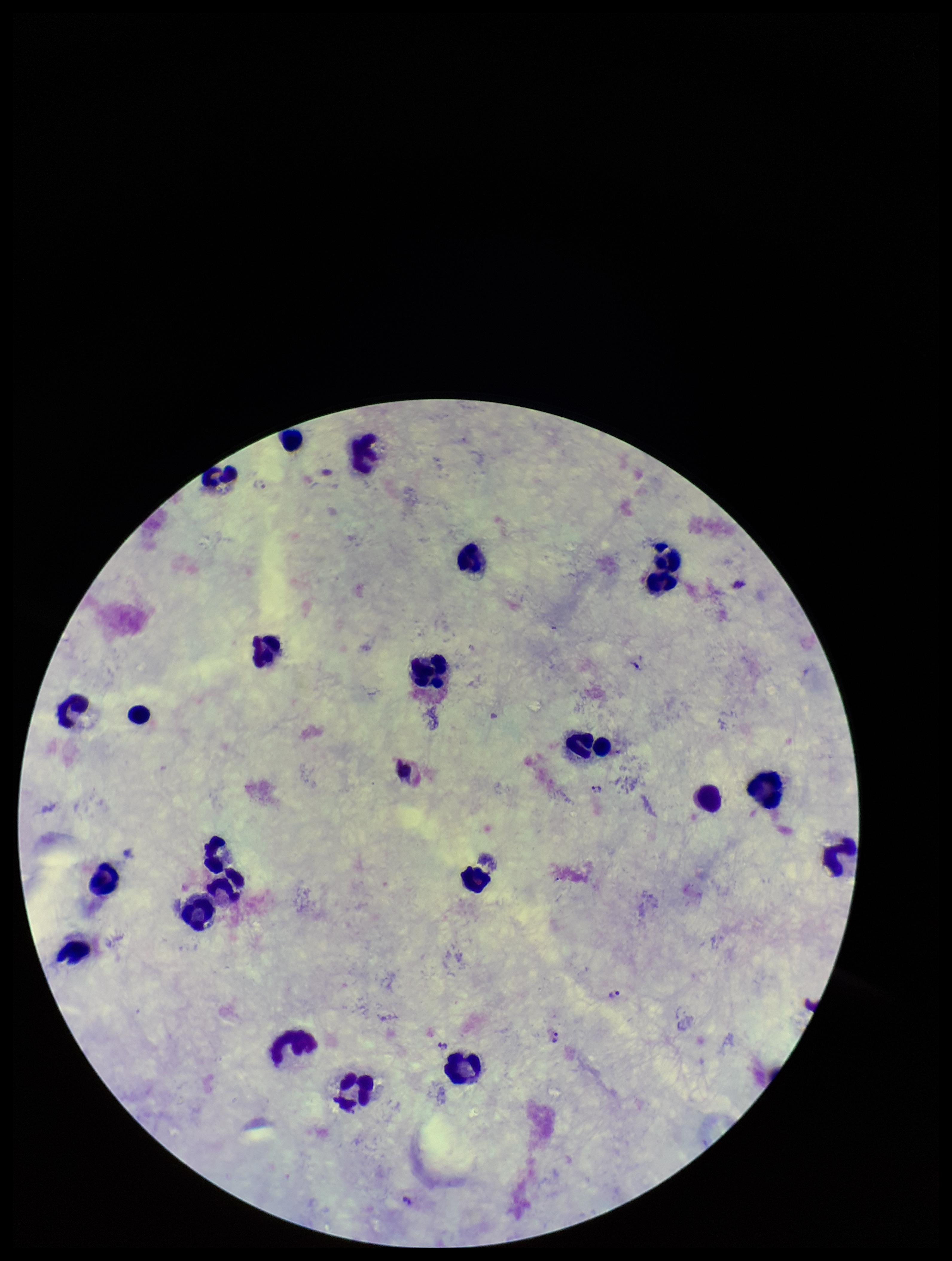
Summary:
  - Plasmodium parasites: seen
  - Patient malaria status: infected
  - Field of view: one from this slide
  - Parasite count: 2
  - Leukocyte count: 23
  - Image size: 952×1261 pixels
  - Species reported for this patient: Plasmodium vivax
  - Preparation: thick smear
  - Stain: Giemsa
  - Capture: smartphone photograph through the microscope eyepiece